Outline each blood parasite and name the species.
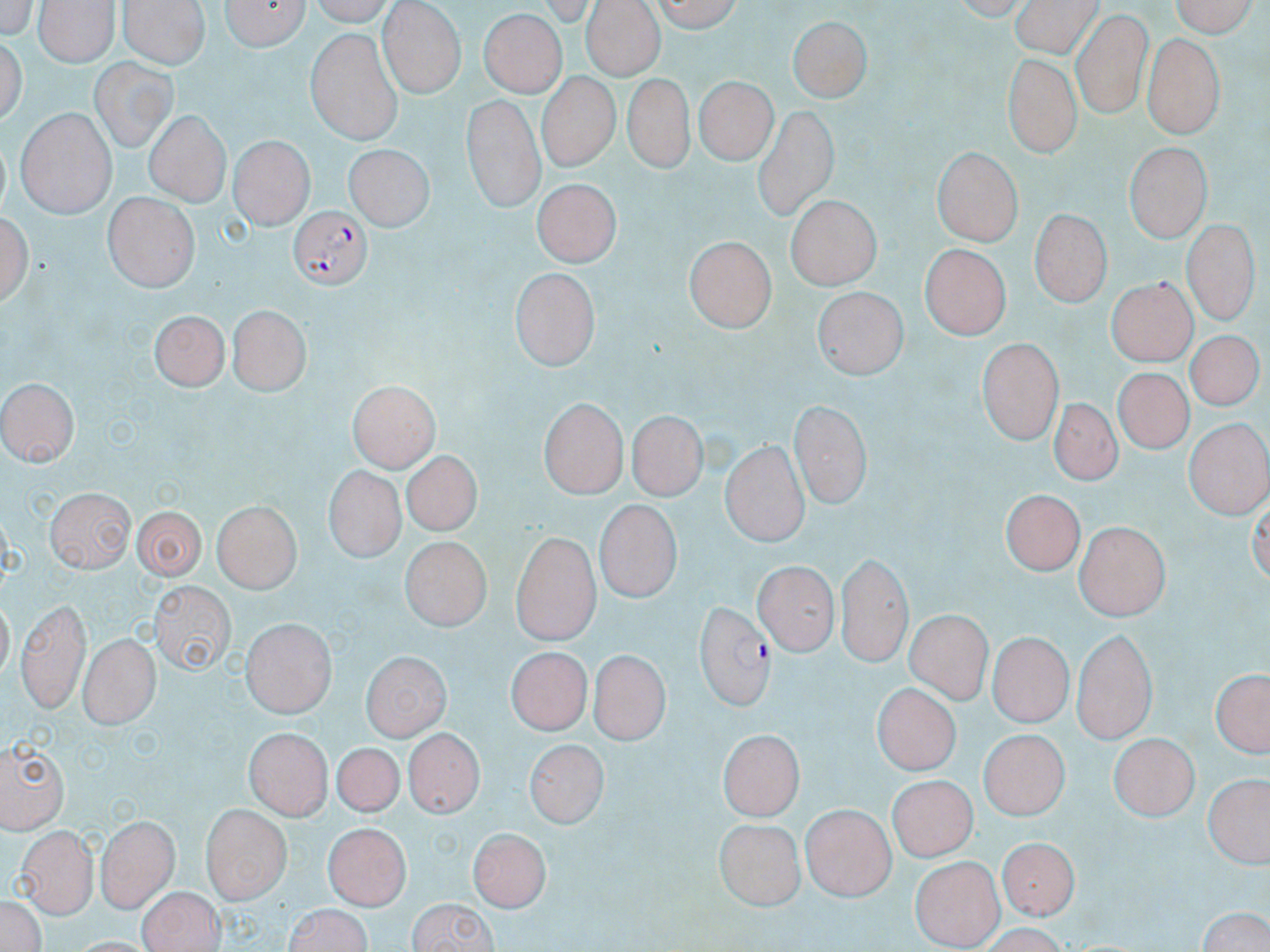

Approximate bounding boxes as named x1/y1/x2/y2 corners in pixels.
Plasmodium falciparum-infected red blood cells: (x1=291, y1=204, x2=373, y2=290), (x1=695, y1=600, x2=775, y2=711).
No Plasmodium ovale, Plasmodium malariae, Plasmodium vivax, Babesia divergens, or Trypanosoma brucei observed.

slide_level_diagnosis: Plasmodium falciparum
image_size: 1270×952 pixels
field_of_view: one of a larger specimen
modality: optical microscopy
preparation: thin blood film
magnification: 1000x
uninfected_red_blood_cell_locations: 'approximate bounding boxes as named x1/y1/x2/y2 corners in pixels: (x1=118, y1=0, x2=211, y2=67), (x1=217, y1=0, x2=311, y2=49), (x1=653, y1=0, x2=741, y2=34), (x1=1009, y1=0, x2=1103, y2=57), (x1=1164, y1=0, x2=1255, y2=35), (x1=39, y1=2, x2=117, y2=67), (x1=579, y1=2, x2=661, y2=80), (x1=379, y1=3, x2=463, y2=97), (x1=481, y1=10, x2=567, y2=99), (x1=1069, y1=11, x2=1153, y2=118), (x1=789, y1=13, x2=873, y2=106), (x1=2, y1=31, x2=29, y2=136), (x1=306, y1=31, x2=403, y2=143), (x1=1143, y1=34, x2=1222, y2=136), (x1=999, y1=54, x2=1080, y2=158), (x1=90, y1=57, x2=175, y2=151), (x1=622, y1=72, x2=694, y2=169), (x1=536, y1=73, x2=616, y2=173), (x1=693, y1=75, x2=775, y2=166), (x1=460, y1=96, x2=545, y2=208), (x1=754, y1=103, x2=840, y2=219), (x1=15, y1=107, x2=117, y2=217), (x1=143, y1=109, x2=229, y2=205), (x1=231, y1=135, x2=315, y2=226), (x1=1121, y1=140, x2=1214, y2=240), (x1=346, y1=145, x2=429, y2=233), (x1=931, y1=146, x2=1022, y2=247), (x1=533, y1=178, x2=621, y2=269), (x1=103, y1=192, x2=198, y2=289), (x1=783, y1=197, x2=878, y2=290), (x1=3, y1=204, x2=35, y2=307), (x1=1028, y1=207, x2=1113, y2=306), (x1=1183, y1=218, x2=1256, y2=324), (x1=683, y1=233, x2=778, y2=333), (x1=921, y1=244, x2=1010, y2=340), (x1=508, y1=266, x2=601, y2=369), (x1=1104, y1=281, x2=1195, y2=367), (x1=811, y1=291, x2=908, y2=380), (x1=229, y1=303, x2=311, y2=393), (x1=152, y1=311, x2=231, y2=388), (x1=1182, y1=334, x2=1260, y2=417), (x1=978, y1=338, x2=1061, y2=445), (x1=1117, y1=365, x2=1192, y2=448), (x1=0, y1=377, x2=76, y2=472), (x1=349, y1=382, x2=437, y2=472), (x1=1045, y1=397, x2=1125, y2=490), (x1=540, y1=399, x2=626, y2=498), (x1=789, y1=399, x2=868, y2=511), (x1=628, y1=411, x2=708, y2=502), (x1=1184, y1=417, x2=1268, y2=515), (x1=721, y1=441, x2=810, y2=548), (x1=399, y1=447, x2=483, y2=540), (x1=322, y1=467, x2=403, y2=566), (x1=43, y1=485, x2=133, y2=572), (x1=1002, y1=486, x2=1088, y2=572), (x1=213, y1=500, x2=300, y2=592), (x1=595, y1=502, x2=679, y2=605), (x1=129, y1=505, x2=208, y2=579), (x1=1076, y1=522, x2=1171, y2=618), (x1=510, y1=530, x2=602, y2=645), (x1=401, y1=540, x2=488, y2=631), (x1=832, y1=553, x2=910, y2=668), (x1=758, y1=559, x2=838, y2=653), (x1=150, y1=579, x2=235, y2=676), (x1=13, y1=597, x2=90, y2=711), (x1=906, y1=610, x2=991, y2=702), (x1=242, y1=617, x2=335, y2=716), (x1=1069, y1=625, x2=1160, y2=743), (x1=991, y1=633, x2=1069, y2=725), (x1=77, y1=636, x2=158, y2=728), (x1=504, y1=644, x2=589, y2=732), (x1=592, y1=645, x2=671, y2=743), (x1=362, y1=651, x2=449, y2=740), (x1=1210, y1=666, x2=1268, y2=759), (x1=873, y1=681, x2=964, y2=772), (x1=408, y1=726, x2=485, y2=815), (x1=244, y1=729, x2=332, y2=818), (x1=718, y1=729, x2=806, y2=818), (x1=981, y1=730, x2=1067, y2=821), (x1=1111, y1=733, x2=1197, y2=822), (x1=523, y1=735, x2=607, y2=827), (x1=2, y1=736, x2=72, y2=832), (x1=323, y1=738, x2=412, y2=829), (x1=1207, y1=771, x2=1269, y2=869), (x1=888, y1=775, x2=978, y2=862), (x1=803, y1=801, x2=897, y2=899), (x1=202, y1=804, x2=291, y2=904), (x1=99, y1=814, x2=177, y2=914), (x1=327, y1=817, x2=407, y2=906), (x1=713, y1=817, x2=803, y2=911), (x1=468, y1=826, x2=550, y2=912), (x1=13, y1=827, x2=97, y2=917), (x1=995, y1=835, x2=1083, y2=919), (x1=913, y1=855, x2=1002, y2=948), (x1=138, y1=883, x2=223, y2=952), (x1=3, y1=892, x2=47, y2=952), (x1=403, y1=898, x2=503, y2=952), (x1=280, y1=903, x2=375, y2=952), (x1=1192, y1=904, x2=1270, y2=952)'
stain: May-Grünwald-Giemsa